Give a bounding box for every leukocyte visible.
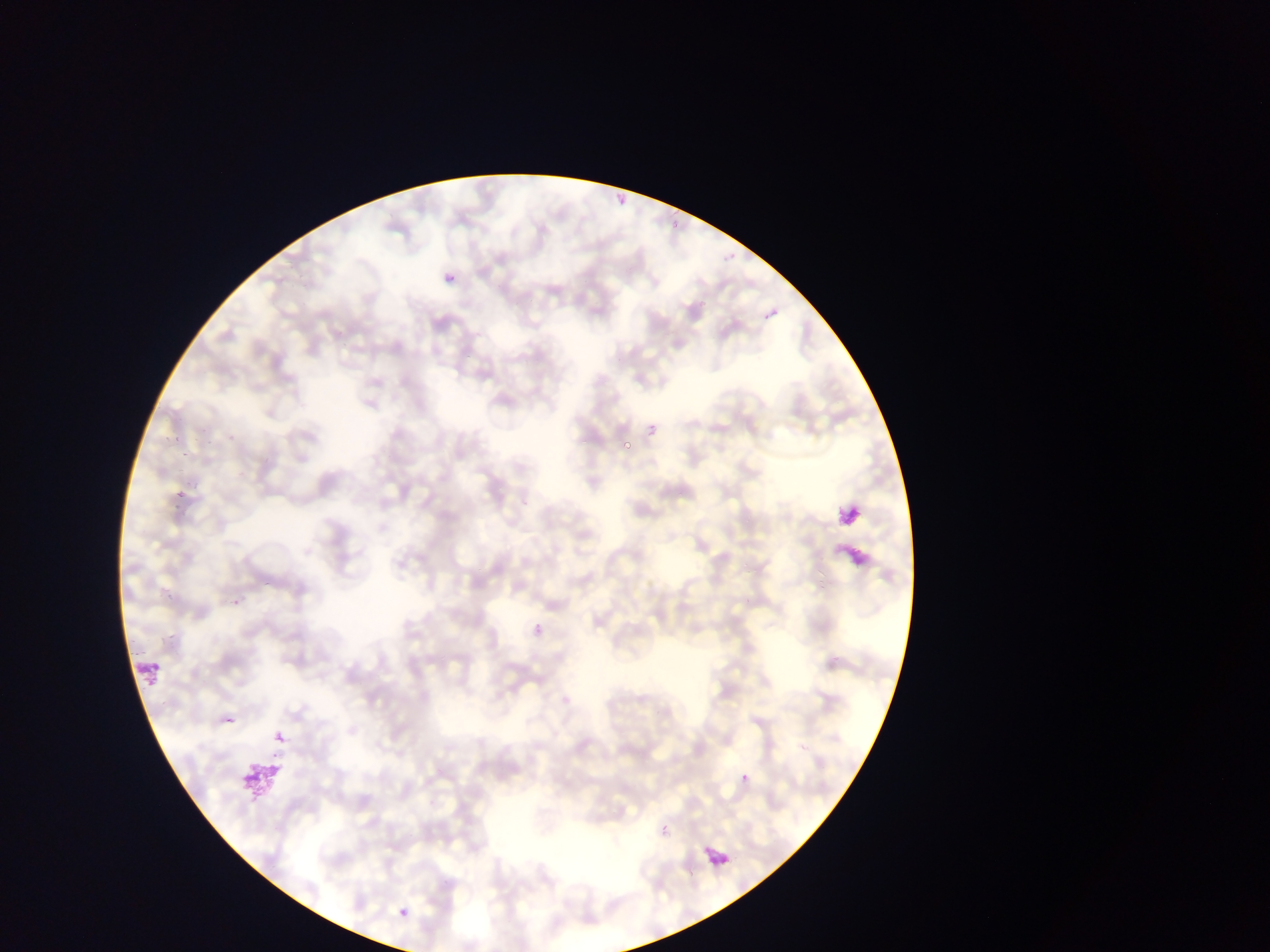
Approximate bounding boxes as [left, top, right, bottom] in pixels.
Leukocytes: [132, 658, 163, 689].

Summary:
  - Plasmodium parasite locations: [445, 274, 457, 284], [762, 307, 777, 321], [647, 422, 659, 435], [622, 440, 632, 450], [833, 499, 865, 529], [275, 733, 286, 744], [741, 773, 750, 783], [661, 825, 669, 834], [703, 845, 732, 871], [398, 908, 408, 918]
  - Preparation: thin blood smear
  - Country: Ghana
  - Image size: 1270×952 pixels
  - Field of view: single
  - Capture: mobile-phone photograph through a microscope